Describe the morphology of the red blood cells.
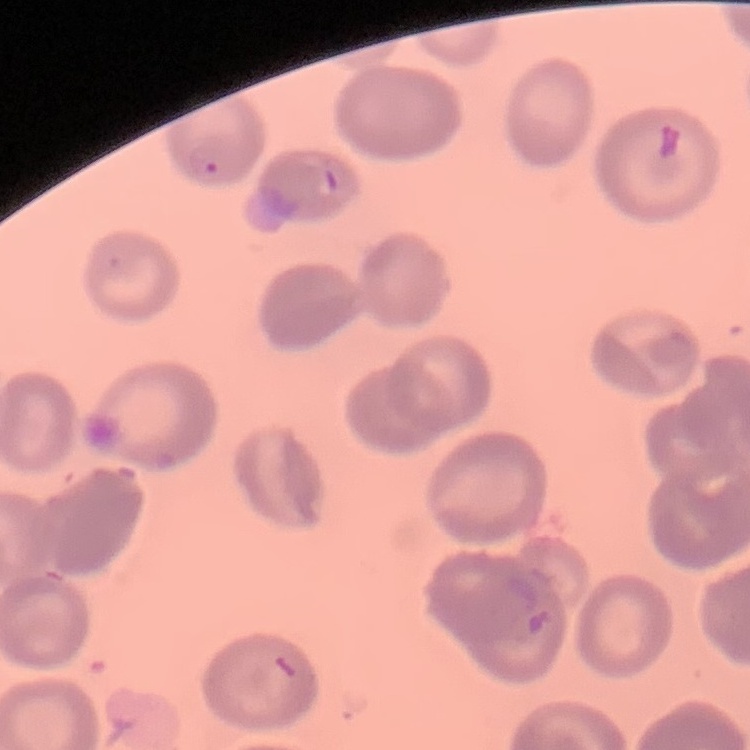

No rouleaux formation.

image type = square crop of a larger photomicrograph
stain = Field's or Giemsa
preparation = thin blood smear